Classify this cell by malaria status.
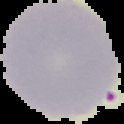
It is uninfected.

Summary:
  - Preparation: thin blood smear
  - Image type: segmented cell region on a black background
  - Image size: 124×124 pixels